Identify the cell.
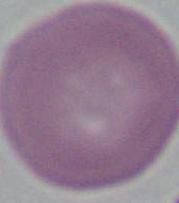
An erythrocyte.

{
  "modality": "photomicrograph",
  "magnification": "1000x"
}